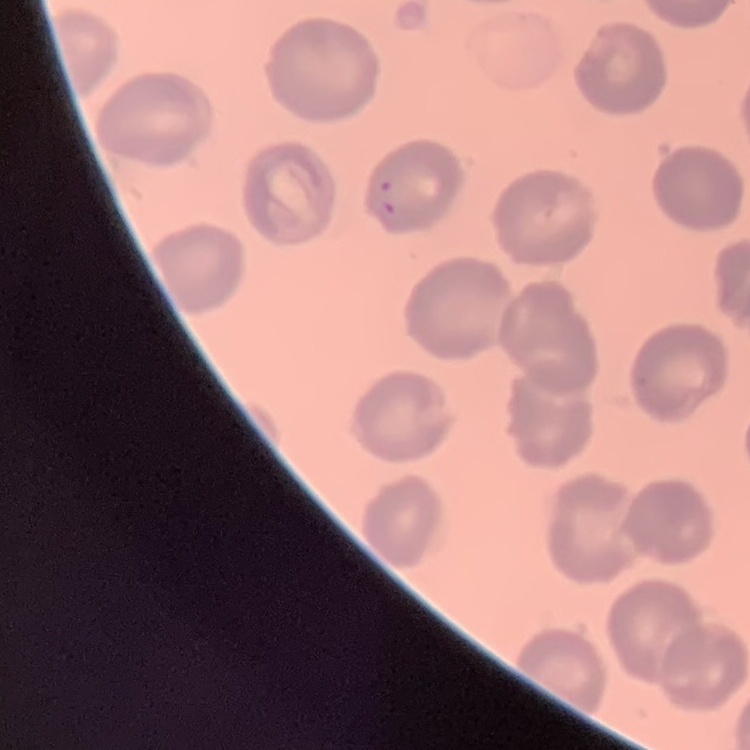
The erythrocytes exhibit no rouleaux formation. Field's or Giemsa stain. Square crop of a larger photomicrograph. Thin peripheral smear.